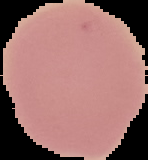

Summary:
  - Image type: segmented cell region with the area outside set to black
  - Result: negative for malaria parasites
  - Preparation: thin blood film
  - Image size: 148×160 pixels